Assess this cell for malaria.
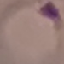

It is parasitized.

Thin blood smear. Acquired by smartphone through the microscope eyepiece. Cell patch, automatically extracted from a larger field of view and resized to 64 × 64 pixels. Giemsa stain.